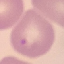

Malaria status: parasitized. Automatically extracted cell patch, resized to 64 × 64 pixels. Photographed with a smartphone camera at the microscope eyepiece. Giemsa stain. Thin blood film.